Assess this cell for malaria.
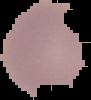

Uninfected.

Summary:
  - Preparation: thin blood film
  - Image type: segmented cell region with the area outside set to black
  - Image size: 91×100 pixels